Assess the morphology of the erythrocytes.
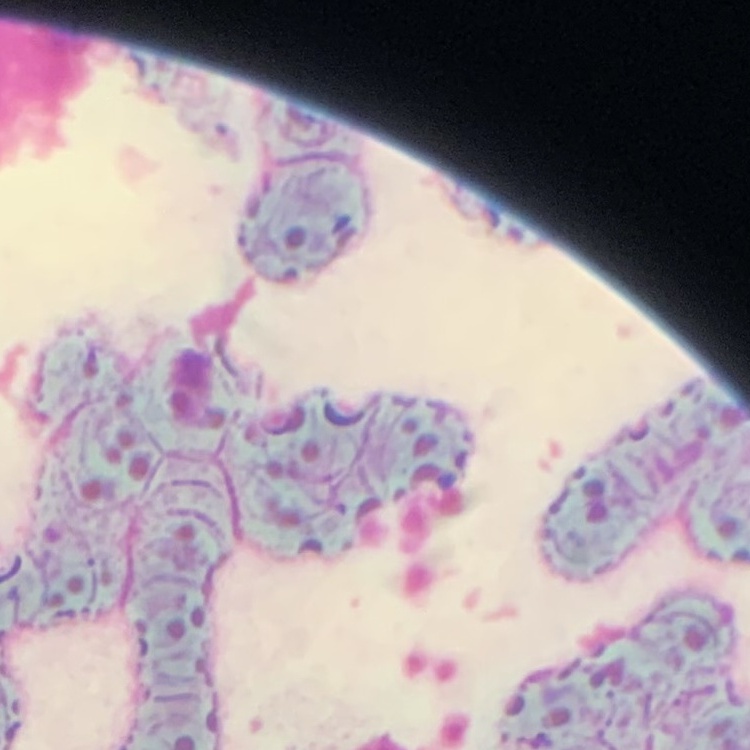

Rouleaux formation.

Stained with either Field's or Giemsa. One tile cut from a larger photomicrograph. Thin peripheral smear.